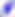

Summary:
  - Identification: Toxoplasma gondii
  - Modality: micrograph
  - Magnification: 400x